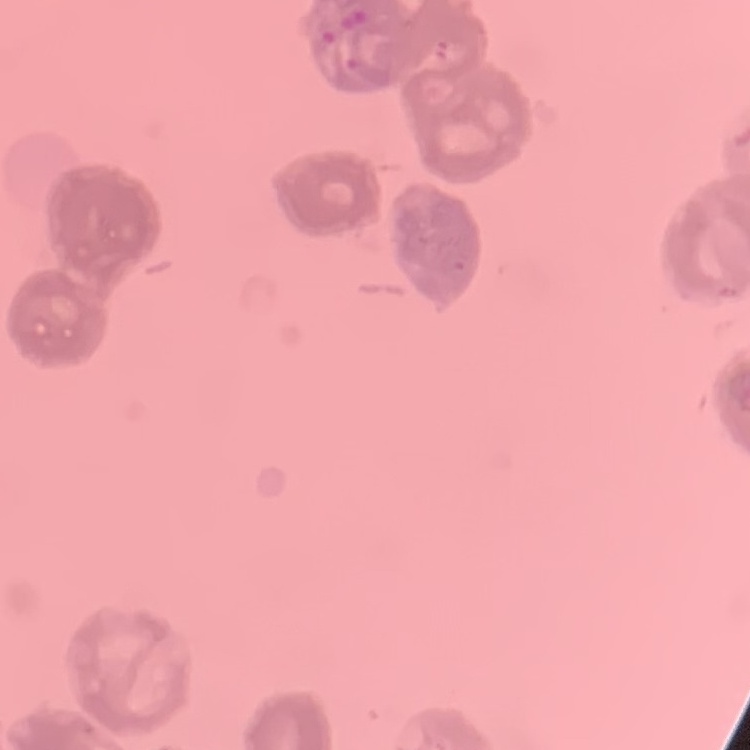
red blood cell morphology = rouleaux formation
preparation = thin blood film
image type = square crop of a larger photomicrograph
stain = Field's or Giemsa